Identify the parasite.
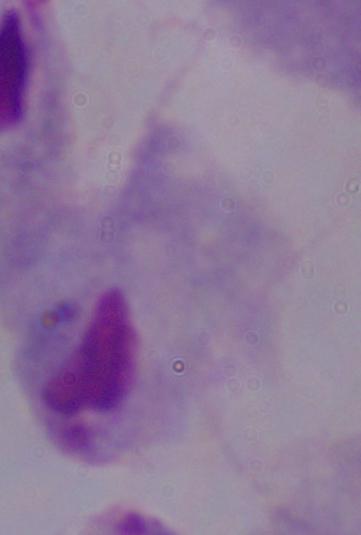
This is a trichomonad.

magnification = 1000x
modality = photomicrograph